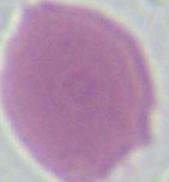
Summary:
  - Modality: micrograph
  - Identification: erythrocyte
  - Magnification: 1000x